Classify this cell by malaria status.
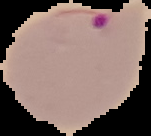
Parasitized.

Summary:
  - Preparation: thin blood smear
  - Image type: segmented cell region on a black background
  - Image size: 151×136 pixels